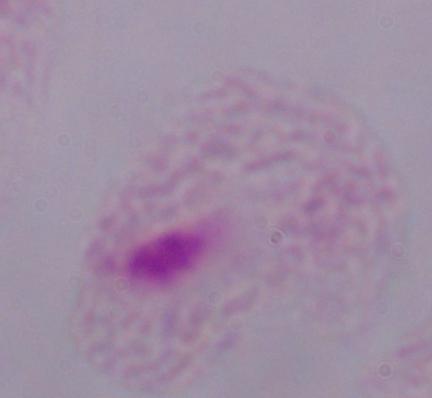 A trichomonad is shown. Micrograph. 1000x magnification.